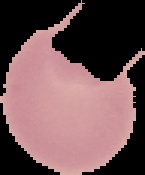
preparation: thin blood smear
malaria_status: uninfected
image_size: 145×175 pixels
image_type: segmented cell region with the area outside set to black